Assess this cell for malaria.
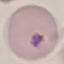

Uninfected.

{
  "capture": "smartphone through the microscope eyepiece",
  "preparation": "thin blood film",
  "image_type": "cell patch, automatically extracted from a larger field of view and resized to 64 × 64 pixels",
  "stain": "Giemsa"
}